Assess this cell for malaria.
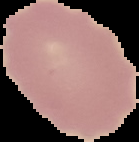
Uninfected.

Summary:
  - Preparation: thin blood film
  - Image size: 139×142 pixels
  - Image type: segmented cell region on a black background